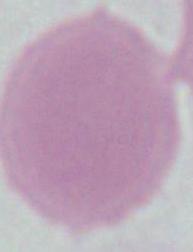
modality = photomicrograph
magnification = 1000x
identification = erythrocyte